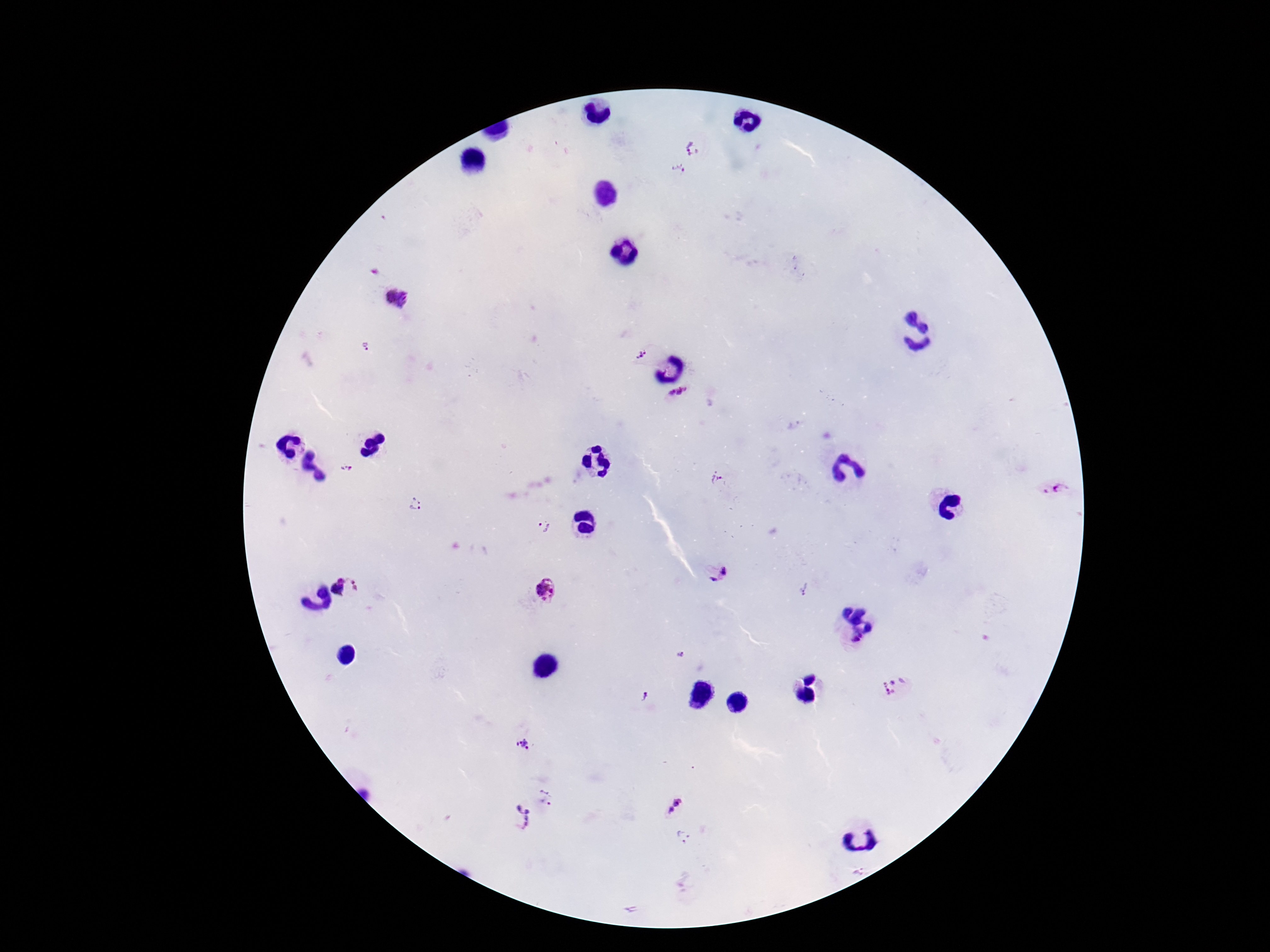

patient malaria status = positive
capture = smartphone camera through the microscope eyepiece
Plasmodium parasite locations = approximate centers as (x, y) in pixels: (693, 150), (678, 170), (398, 298), (365, 348), (640, 354), (678, 394), (346, 468), (717, 478), (1053, 488), (416, 505), (543, 525), (724, 571), (341, 579), (713, 580), (354, 585), (546, 589), (804, 589), (337, 590), (855, 641), (681, 656), (891, 686), (642, 696), (524, 745), (546, 796), (678, 802), (669, 810), (519, 818), (683, 836), (857, 870)
image size = 1270×952 pixels
field of view = single
stain = Giemsa
magnification = 100x
preparation = thick blood film